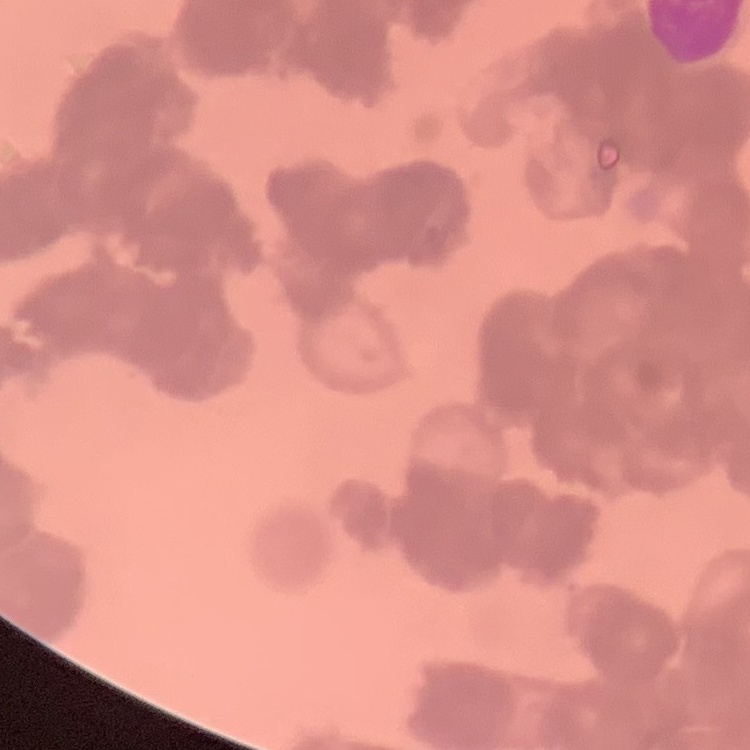 The red blood cells show rouleaux formation. Thin peripheral smear. Stained with either Field's or Giemsa. Square crop of a larger photomicrograph.